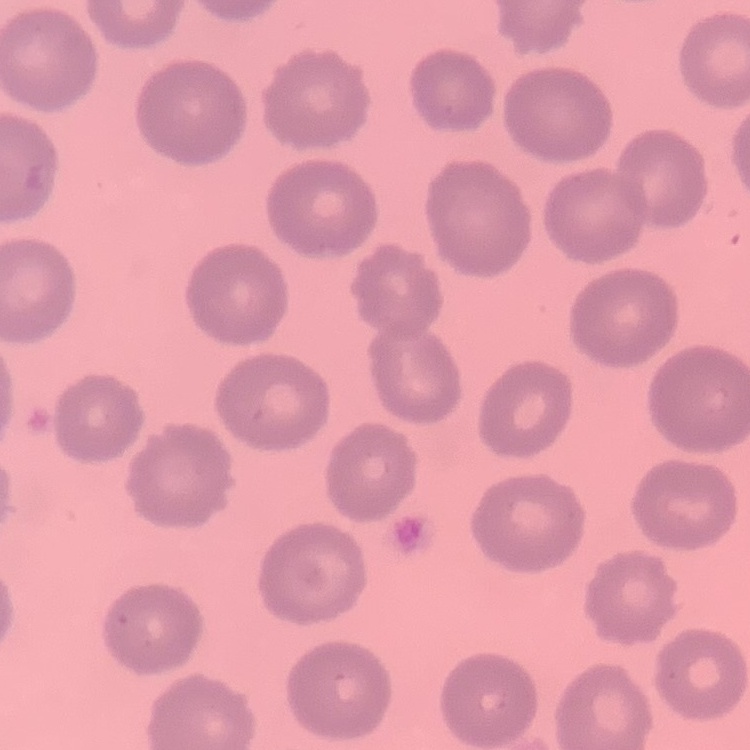

erythrocyte morphology = no rouleaux formation
preparation = thin blood film
stain = Field's or Giemsa
image type = one tile cut from a larger photomicrograph